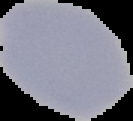
image size = 133×121 pixels
preparation = thin blood smear
malaria status = uninfected
image type = segmented cell region with the area outside set to black